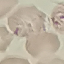
{
  "malaria_status": "uninfected",
  "preparation": "thin blood smear",
  "stain": "Giemsa",
  "capture": "smartphone through the microscope eyepiece",
  "image_type": "cell patch, automatically extracted from a larger field of view and resized to 64 × 64 pixels"
}